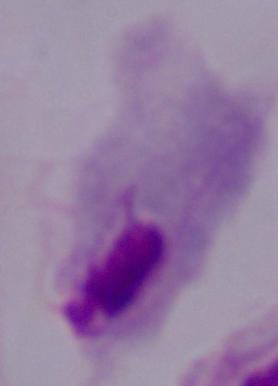

Micrograph. A trichomonad is seen. Captured at 1000x magnification.